Comment on the morphology of the red blood cells.
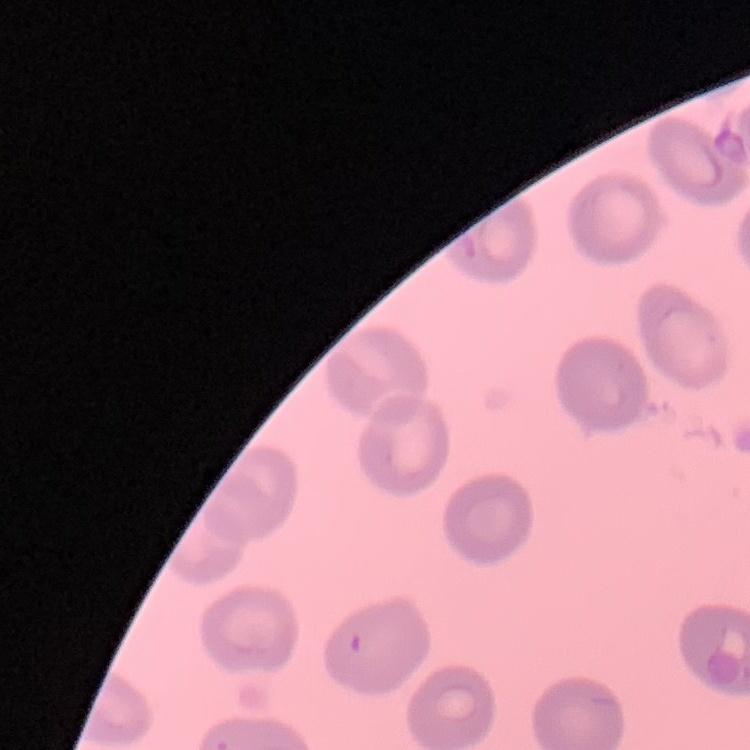
They show no rouleaux formation.

preparation = thin peripheral smear
image type = square crop of a larger photomicrograph
stain = Field's or Giemsa